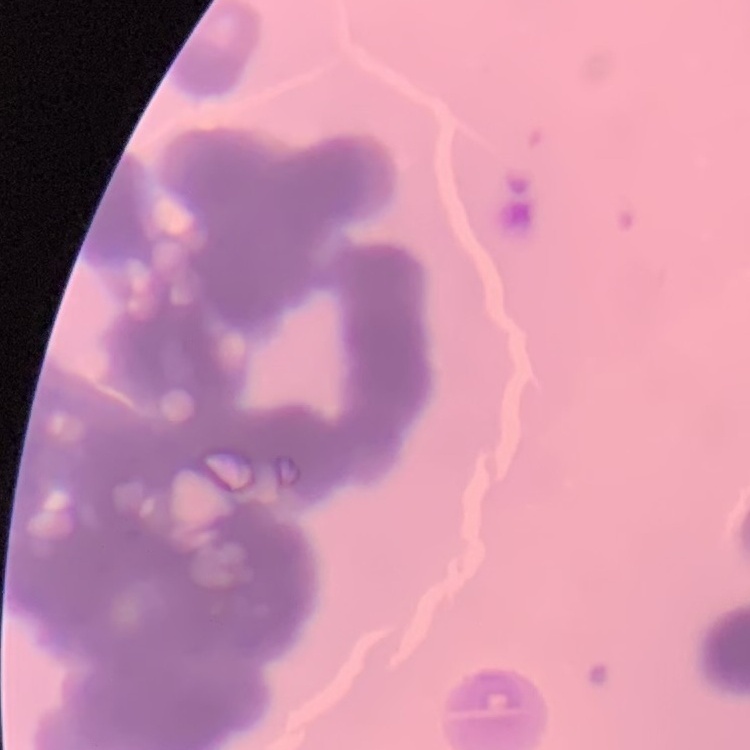
red_blood_cell_morphology: rouleaux formation
preparation: thin blood film
stain: Field's or Giemsa
image_type: square crop of a larger photomicrograph